State the blood parasite species.
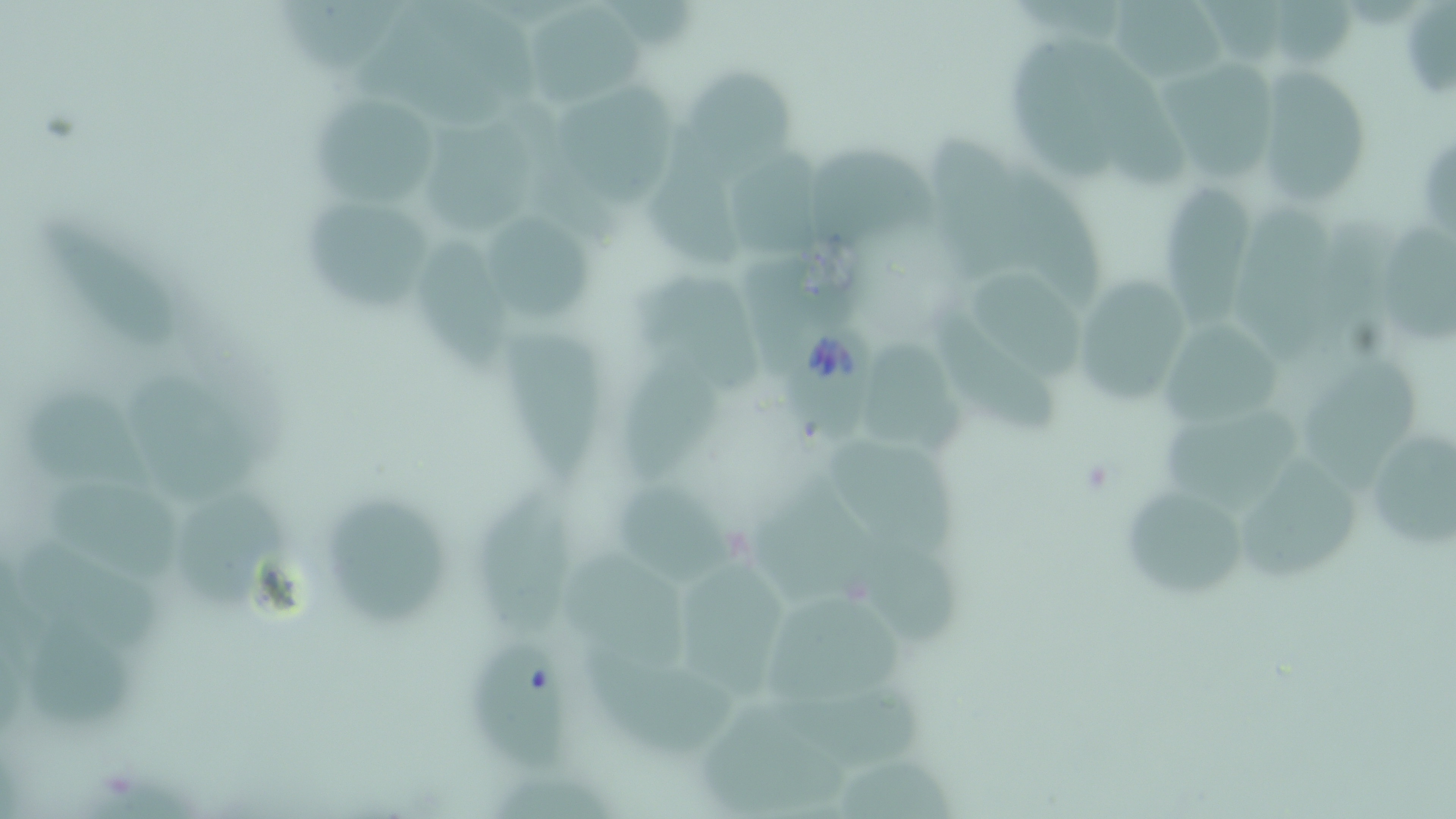

Babesia divergens.

preparation: thin blood film
uninfected_red_blood_cell_locations: 'approximate bounding boxes as [x1, y1, x2, y2] in pixels: [280, 0, 405, 79], [1108, 0, 1229, 87], [1266, 0, 1359, 69], [519, 1, 645, 109], [350, 2, 544, 129], [1400, 5, 1456, 102], [1011, 31, 1135, 190], [1153, 56, 1278, 188], [687, 62, 800, 191], [1256, 68, 1375, 207], [551, 83, 672, 211], [309, 94, 444, 205], [425, 116, 543, 240], [920, 123, 1039, 285], [1420, 139, 1456, 239], [646, 143, 754, 275], [809, 147, 939, 258], [730, 148, 829, 259], [1006, 165, 1109, 311], [1152, 185, 1257, 333], [298, 199, 438, 313], [1231, 204, 1334, 374], [37, 211, 187, 352], [486, 214, 598, 321], [1386, 228, 1456, 346], [420, 233, 511, 382], [966, 270, 1088, 381], [632, 271, 768, 397], [1083, 273, 1190, 405], [936, 304, 1060, 438], [1158, 320, 1287, 426], [504, 330, 607, 488], [617, 335, 720, 490], [868, 335, 973, 453], [1295, 351, 1419, 496], [123, 375, 269, 509], [23, 383, 162, 499], [1160, 404, 1306, 515], [1362, 423, 1456, 558], [828, 433, 965, 566], [1241, 453, 1360, 581], [748, 465, 886, 602], [43, 473, 186, 588], [617, 477, 741, 592], [472, 483, 574, 637], [1115, 484, 1254, 599], [323, 490, 452, 628], [173, 493, 294, 609], [859, 530, 967, 649], [19, 532, 171, 659], [567, 549, 693, 671], [686, 555, 789, 708], [761, 587, 909, 711], [23, 619, 143, 738], [469, 637, 571, 780], [580, 642, 741, 756], [768, 687, 936, 774], [699, 703, 855, 814], [839, 756, 960, 816]'
field_of_view: single
image_size: 1456×819 pixels
babesia_divergens_infected_red_blood_cell_locations: 'approximate bounding boxes as [x1, y1, x2, y2] in pixels: [775, 298, 879, 443]'
magnification: 1000x
stain: May-Grünwald-Giemsa
modality: optical microscopy